Classify this cell by malaria status.
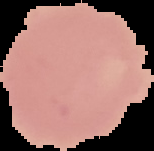

It is uninfected.

Cell region segmented out of the field of view; the surrounding area is masked to black. From a thin blood smear. Image is 154×151 pixels.